Locate every blood parasite and identify its species.
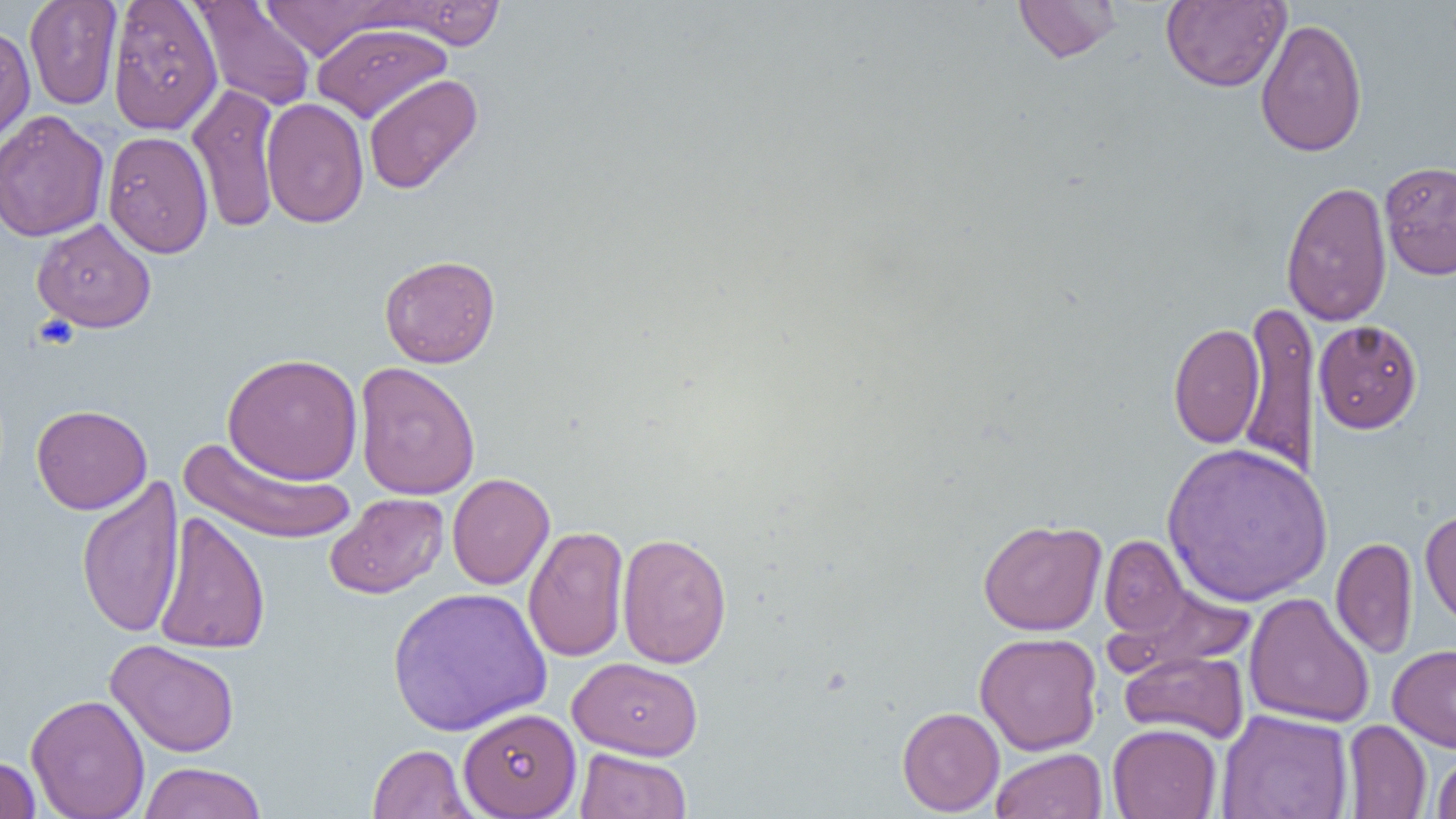
No blood parasites seen.

slide-level diagnosis = negative for blood parasites
image size = 1456×819 pixels
magnification = 1000x
uninfected red blood cell locations = approximate bounding boxes as named x1/y1/x2/y2 corners in pixels: (x1=24, y1=0, x2=123, y2=110), (x1=107, y1=0, x2=223, y2=135), (x1=1013, y1=0, x2=1122, y2=63), (x1=1161, y1=0, x2=1290, y2=91), (x1=192, y1=1, x2=317, y2=112), (x1=258, y1=1, x2=399, y2=61), (x1=373, y1=1, x2=508, y2=49), (x1=1175, y1=4, x2=1361, y2=118), (x1=1255, y1=17, x2=1368, y2=157), (x1=0, y1=23, x2=35, y2=154), (x1=311, y1=23, x2=452, y2=123), (x1=363, y1=74, x2=482, y2=195), (x1=187, y1=83, x2=281, y2=233), (x1=261, y1=97, x2=369, y2=228), (x1=0, y1=110, x2=110, y2=242), (x1=101, y1=130, x2=213, y2=258), (x1=1379, y1=160, x2=1456, y2=280), (x1=1281, y1=180, x2=1393, y2=327), (x1=32, y1=217, x2=156, y2=333), (x1=379, y1=254, x2=500, y2=368), (x1=1238, y1=297, x2=1319, y2=483), (x1=1313, y1=320, x2=1423, y2=434), (x1=1168, y1=322, x2=1265, y2=449), (x1=222, y1=353, x2=363, y2=485), (x1=354, y1=361, x2=481, y2=501), (x1=31, y1=404, x2=152, y2=515), (x1=178, y1=437, x2=358, y2=545), (x1=1161, y1=440, x2=1333, y2=607), (x1=447, y1=472, x2=555, y2=590), (x1=76, y1=475, x2=185, y2=640), (x1=325, y1=492, x2=449, y2=599), (x1=1420, y1=508, x2=1456, y2=631), (x1=153, y1=510, x2=271, y2=656), (x1=977, y1=518, x2=1106, y2=635), (x1=523, y1=525, x2=630, y2=663), (x1=617, y1=532, x2=732, y2=669), (x1=1098, y1=535, x2=1191, y2=639), (x1=1331, y1=537, x2=1417, y2=660), (x1=1106, y1=581, x2=1255, y2=674), (x1=388, y1=586, x2=552, y2=736), (x1=1244, y1=592, x2=1375, y2=728), (x1=975, y1=631, x2=1102, y2=755), (x1=105, y1=639, x2=240, y2=757), (x1=1388, y1=644, x2=1456, y2=753), (x1=1119, y1=650, x2=1249, y2=743), (x1=567, y1=657, x2=703, y2=760), (x1=26, y1=693, x2=150, y2=819), (x1=896, y1=706, x2=1005, y2=816), (x1=458, y1=707, x2=581, y2=818), (x1=1216, y1=709, x2=1354, y2=819), (x1=1342, y1=719, x2=1432, y2=818), (x1=1107, y1=723, x2=1222, y2=819), (x1=367, y1=744, x2=478, y2=819), (x1=575, y1=748, x2=692, y2=819), (x1=991, y1=748, x2=1107, y2=819), (x1=1431, y1=750, x2=1456, y2=818), (x1=0, y1=755, x2=41, y2=818), (x1=138, y1=762, x2=267, y2=819)
modality = light microscopy
preparation = thin blood film
field of view = single
platelet locations = approximate bounding boxes as named x1/y1/x2/y2 corners in pixels: (x1=33, y1=315, x2=78, y2=352)